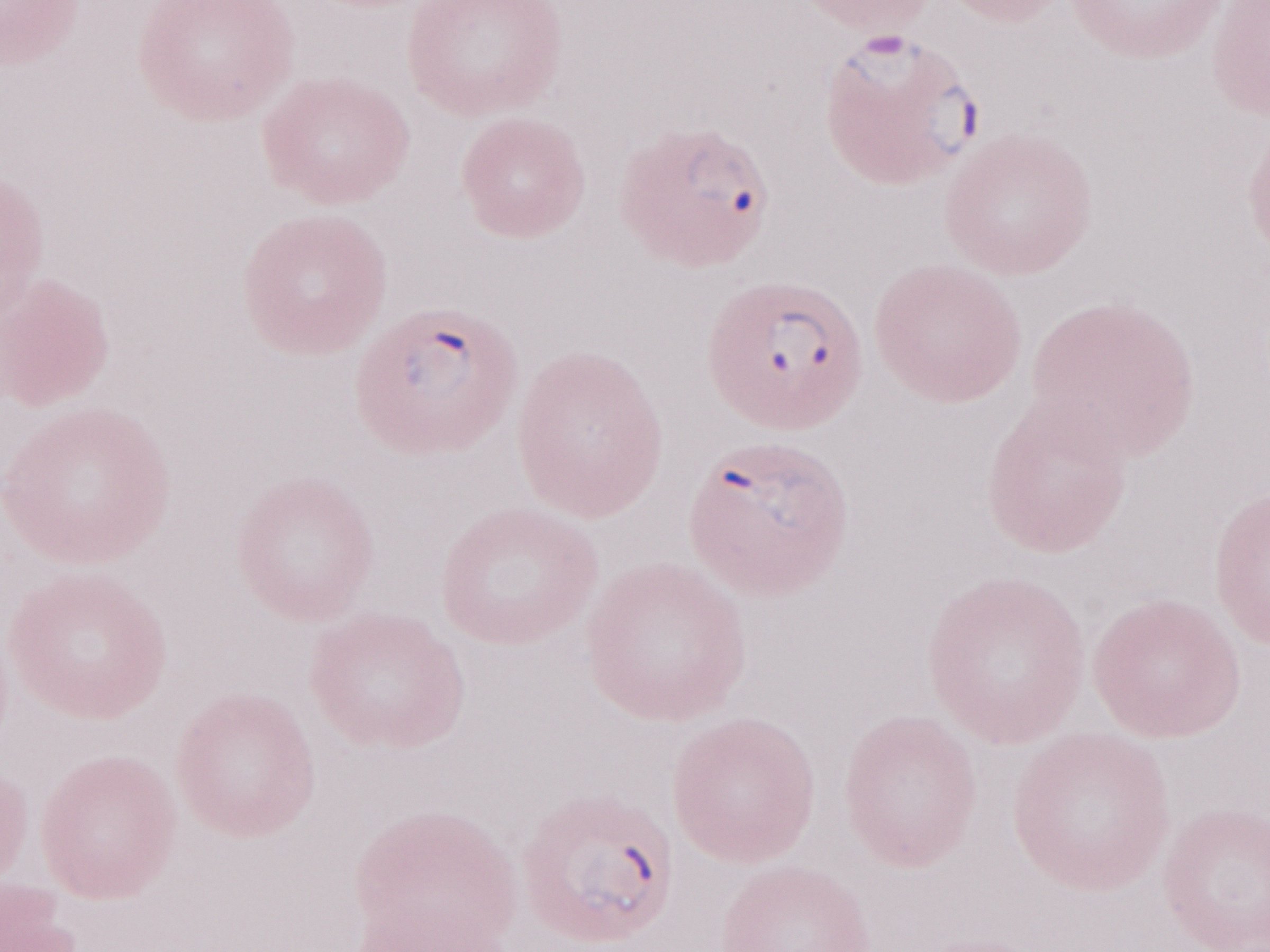 Malaria diagnosis (patient-level): positive. One field of this slide. Thin blood smear. May-Grünwald-Giemsa stain. Image is 1270×952 pixels. Olympus BX43 microscope, Olympus DP73 camera. 1,000x magnification.